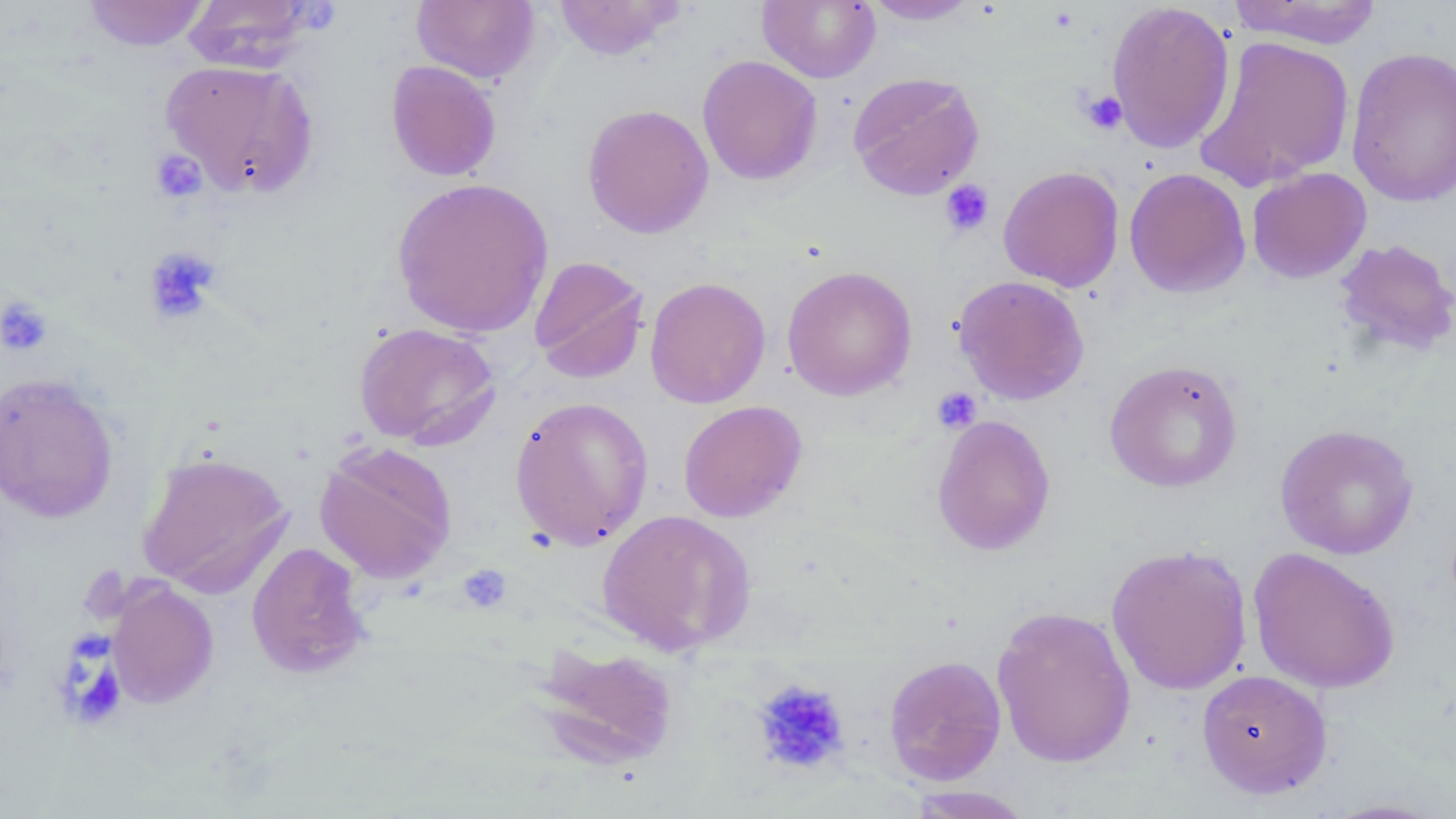

Summary:
  - Coordinate format: approximate bounding boxes as [x1, y1, x2, y2] in pixels
  - Uninfected red blood cell locations: [83, 0, 209, 51], [182, 0, 320, 72], [411, 0, 540, 84], [553, 0, 685, 60], [757, 0, 880, 83], [861, 0, 982, 25], [1228, 0, 1383, 48], [1105, 1, 1235, 154], [1195, 34, 1355, 191], [1345, 46, 1456, 207], [697, 55, 823, 186], [160, 59, 319, 200], [385, 60, 502, 182], [847, 71, 985, 200], [582, 103, 714, 239], [998, 165, 1125, 292], [1124, 167, 1251, 298], [1247, 167, 1371, 283], [390, 176, 555, 339], [1333, 238, 1456, 358], [528, 256, 650, 384], [782, 265, 918, 401], [952, 275, 1090, 405], [645, 276, 771, 408], [353, 322, 501, 449], [1104, 359, 1243, 493], [0, 372, 120, 523], [509, 395, 654, 550], [678, 400, 808, 523], [931, 414, 1056, 556], [1274, 424, 1419, 559], [314, 442, 457, 583], [135, 450, 294, 597], [596, 509, 756, 656], [246, 541, 370, 680], [1106, 543, 1253, 695], [1248, 547, 1401, 693], [106, 579, 219, 708], [991, 604, 1137, 768], [533, 642, 680, 771], [883, 654, 1007, 786], [1196, 669, 1332, 799], [902, 786, 1037, 818], [1319, 798, 1452, 818]
  - Platelet locations: [1078, 90, 1127, 135], [150, 149, 207, 203], [939, 180, 994, 236], [143, 246, 221, 324], [1, 296, 52, 356], [932, 386, 982, 434], [458, 565, 511, 613], [67, 635, 123, 722], [751, 679, 850, 776]
  - Slide-level diagnosis: no evidence of blood parasites
  - Modality: light microscopy
  - Magnification: 1000x
  - Image size: 1456×819 pixels
  - Field of view: single
  - Stain: May-Grünwald-Giemsa
  - Preparation: thin blood film